Report the malaria status of this cell.
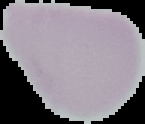
It is uninfected.

image_type: cell region segmented out of the field of view; surrounding area masked to black
preparation: thin blood film
image_size: 145×124 pixels